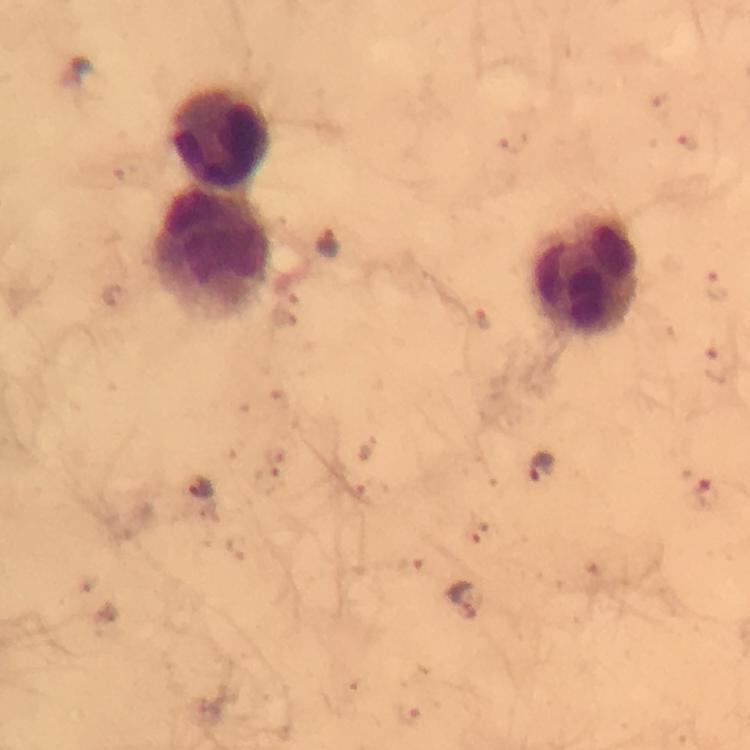
{
  "capture": "smartphone photograph through a microscope",
  "image_size": "750×750 pixels",
  "malaria_parasite_locations": "approximate centers as [x, y] in pixels: [327, 242], [540, 466], [199, 487], [707, 491], [463, 601]",
  "cropped_from": "one field of view",
  "immersion_oil": "used",
  "leukocyte_locations": "approximate centers as [x, y] in pixels: [221, 136], [213, 250], [585, 274]",
  "stain": "Giemsa",
  "context": "from a diagnostic examination for malaria",
  "magnification": "100x",
  "preparation": "thick blood film"
}